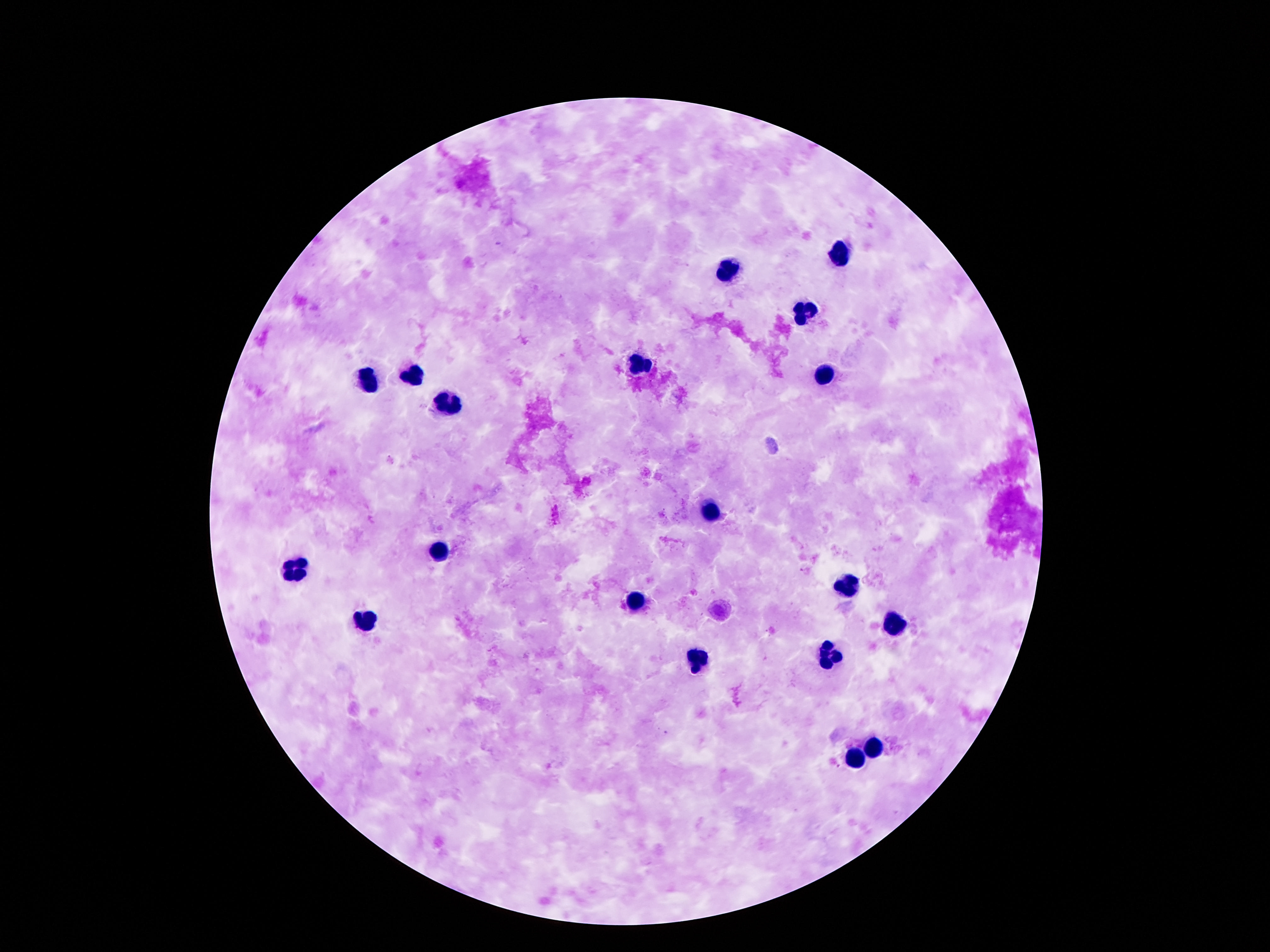
Approximate object centers, in pixels from the top-left corner. Leukocyte locations: (x=841, y=254), (x=727, y=268), (x=806, y=315), (x=641, y=366), (x=412, y=375), (x=368, y=378), (x=821, y=378), (x=445, y=399), (x=711, y=511), (x=442, y=551), (x=295, y=568), (x=846, y=587), (x=636, y=602), (x=365, y=621), (x=893, y=625), (x=832, y=655), (x=701, y=658), (x=876, y=742), (x=856, y=760). Giemsa-stained preparation. Image is 1270×952 pixels. 100x magnification. One field from this slide. Thick blood smear. Patient malaria status: not infected. Smartphone photograph taken through the microscope eyepiece.